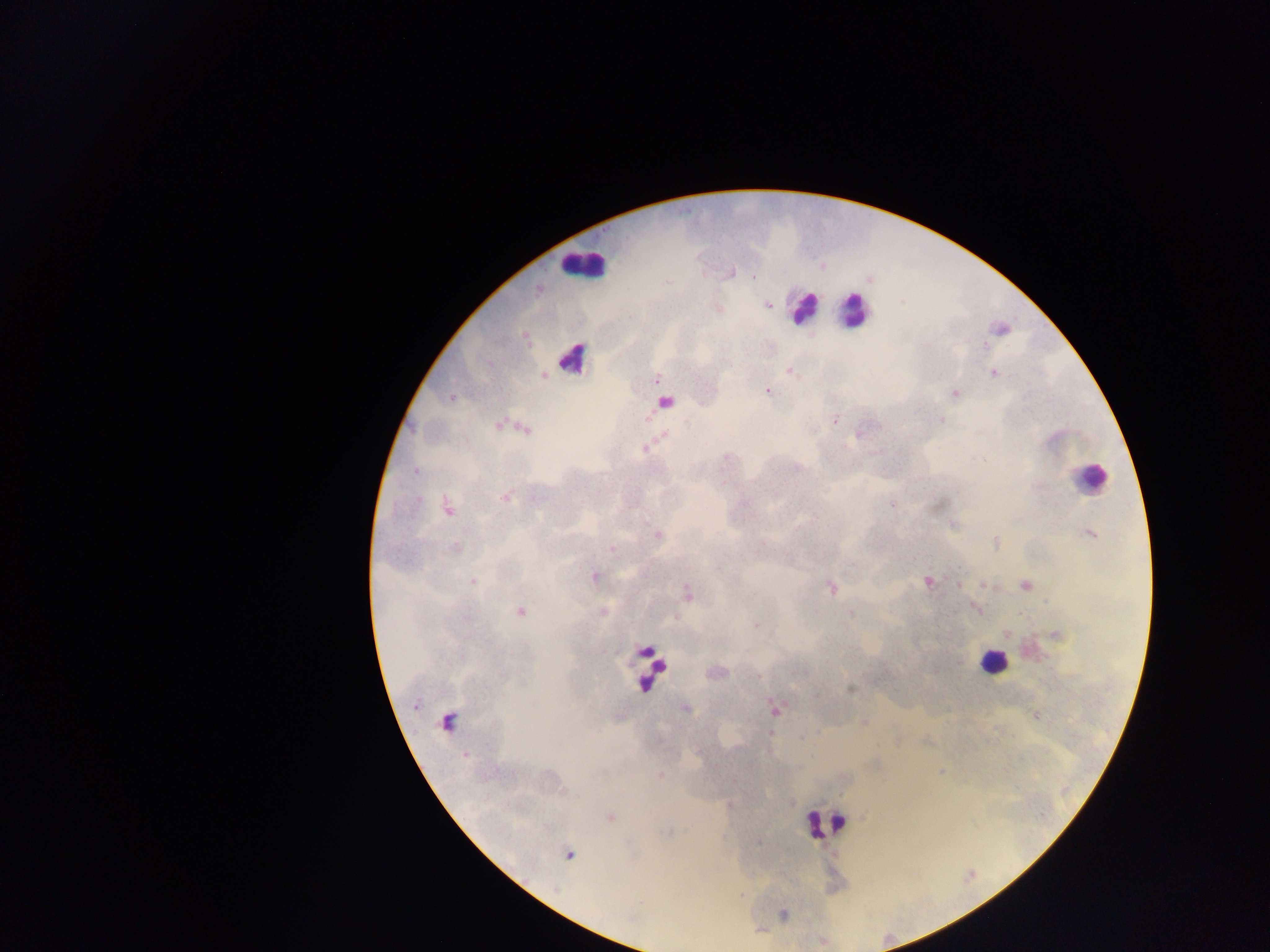

Approximate centers as {x, y} in pixels.
Summary:
  - Leukocyte locations (subset; some below the resolvable size): {582, 265}, {803, 307}, {852, 312}, {572, 358}, {1088, 477}, {993, 662}, {650, 667}, {448, 725}, {825, 823}
  - Plasmodium parasite locations: {767, 305}, {789, 370}, {994, 373}, {656, 379}, {767, 390}, {955, 394}, {451, 397}, {835, 420}, {941, 420}, {497, 425}, {526, 431}, {663, 434}, {646, 447}, {415, 472}, {506, 496}, {418, 500}, {893, 504}, {448, 510}, {1090, 534}, {658, 535}, {612, 548}, {454, 549}, {594, 576}, {473, 581}, {928, 582}, {958, 584}, {1026, 585}, {830, 588}, {687, 592}, {520, 611}, {602, 612}, {757, 625}, {850, 689}, {415, 704}, {685, 708}, {775, 709}, {1035, 715}, {771, 733}, {609, 816}, {569, 855}
  - Preparation: thick blood film
  - Country: Ghana
  - Capture: mobile-phone photograph through a microscope
  - Field of view: single
  - Image size: 1270×952 pixels